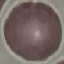

result = no malaria parasites detected
stain = Giemsa
image type = cell patch, automatically extracted from a larger field of view and resized to 64 × 64 pixels
capture = smartphone through the microscope eyepiece
preparation = thin smear